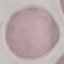

Summary:
  - Result: negative for malaria parasites
  - Capture: smartphone through the microscope eyepiece
  - Preparation: thin blood smear
  - Stain: Giemsa
  - Image type: automatically extracted cell patch, resized to 64 × 64 pixels